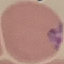

Malaria status: uninfected. Giemsa-stained preparation. Photographed with a smartphone camera at the microscope eyepiece. Thin smear of blood. Cell patch, automatically extracted from a larger field of view and resized to 64 × 64 pixels.